State which cell type is depicted.
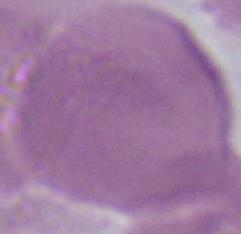
This is an erythrocyte.

Micrograph. Captured at 1000x magnification.